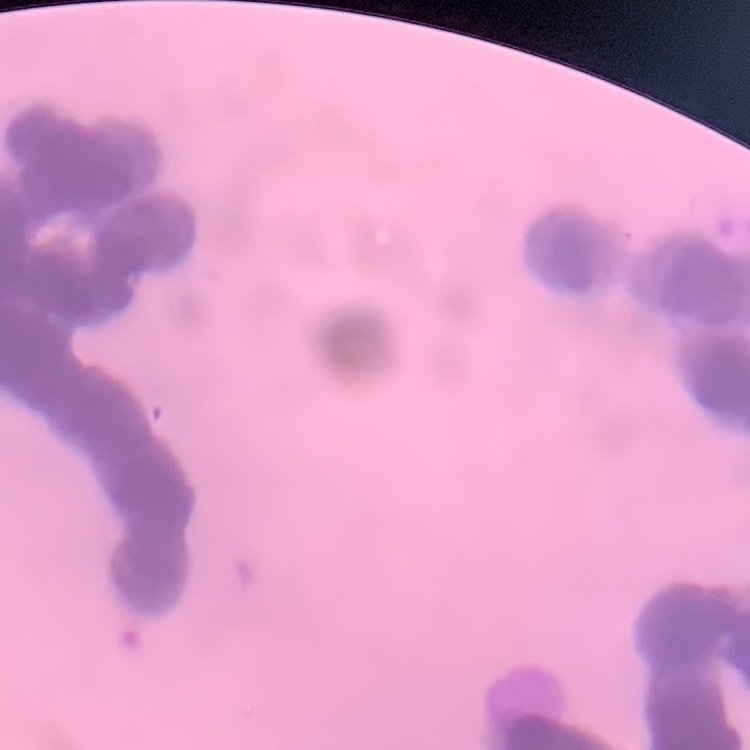
The erythrocytes show rouleaux formation. Field's or Giemsa stain. Thin blood film. Square crop of a larger photomicrograph.